Comment on the morphology of the erythrocytes.
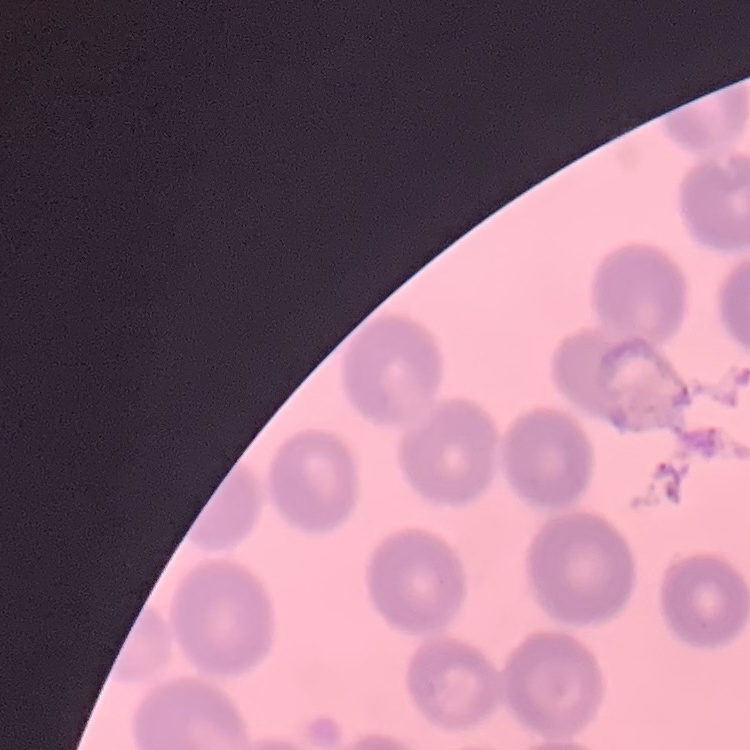

No rouleaux formation.

stain: Field's or Giemsa
preparation: thin blood smear
image_type: square crop of a larger photomicrograph